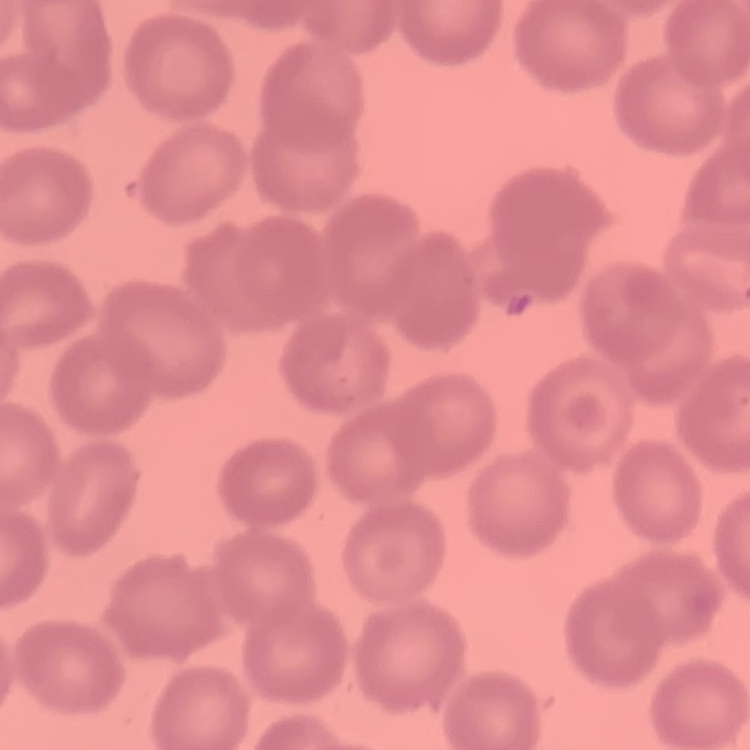
red blood cell morphology = no rouleaux formation
image type = square crop of a larger photomicrograph
preparation = thin blood film
stain = Field's or Giemsa